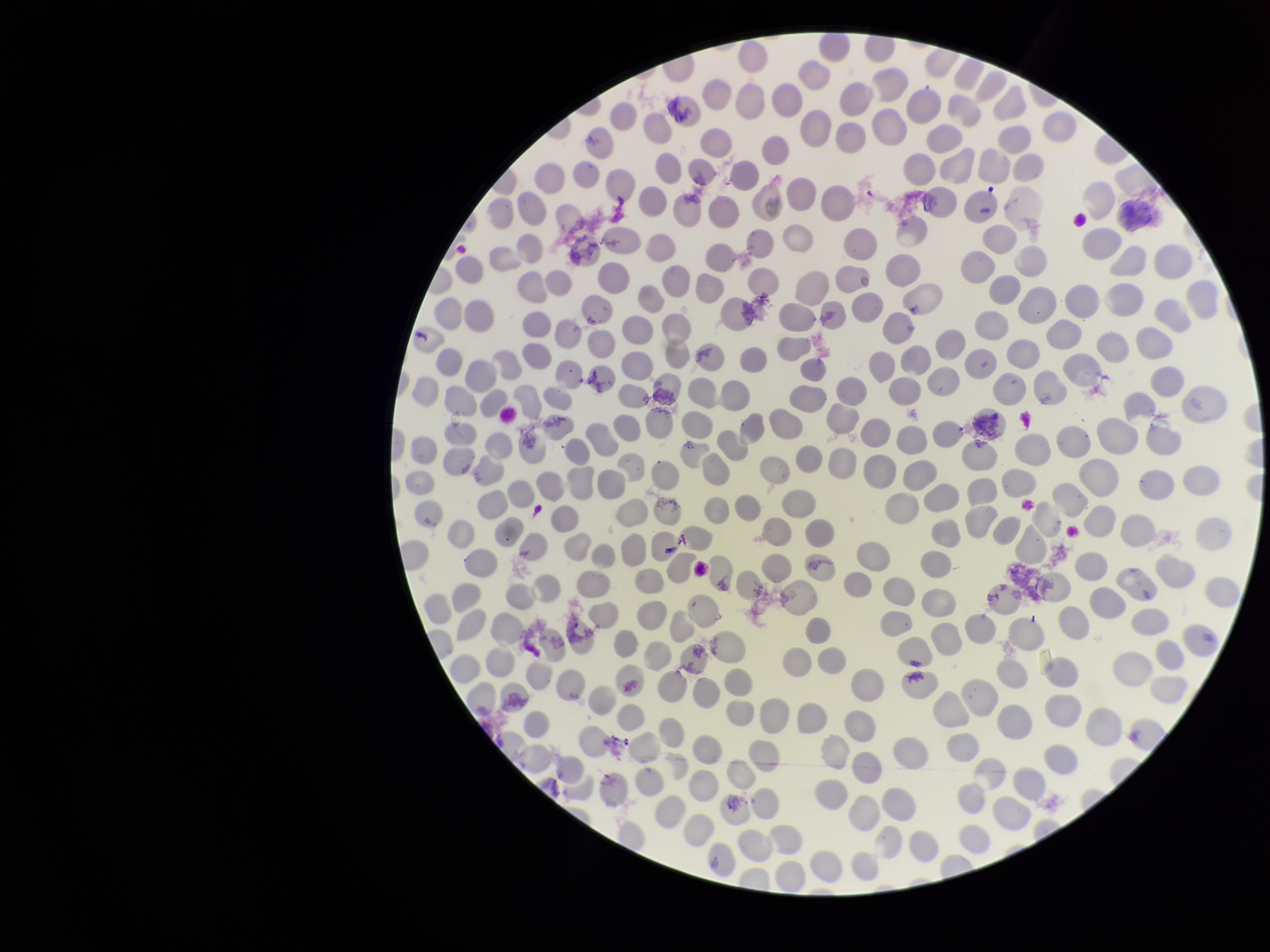
patient_malaria_status: negative
parasitized_red_blood_cells: none seen
parasitized_red_blood_cell_count: 0
red_blood_cell_count: 323
preparation: thin blood smear
image_size: 1270×952 pixels
field_of_view: single
stain: Giemsa
capture: smartphone photograph through the microscope eyepiece